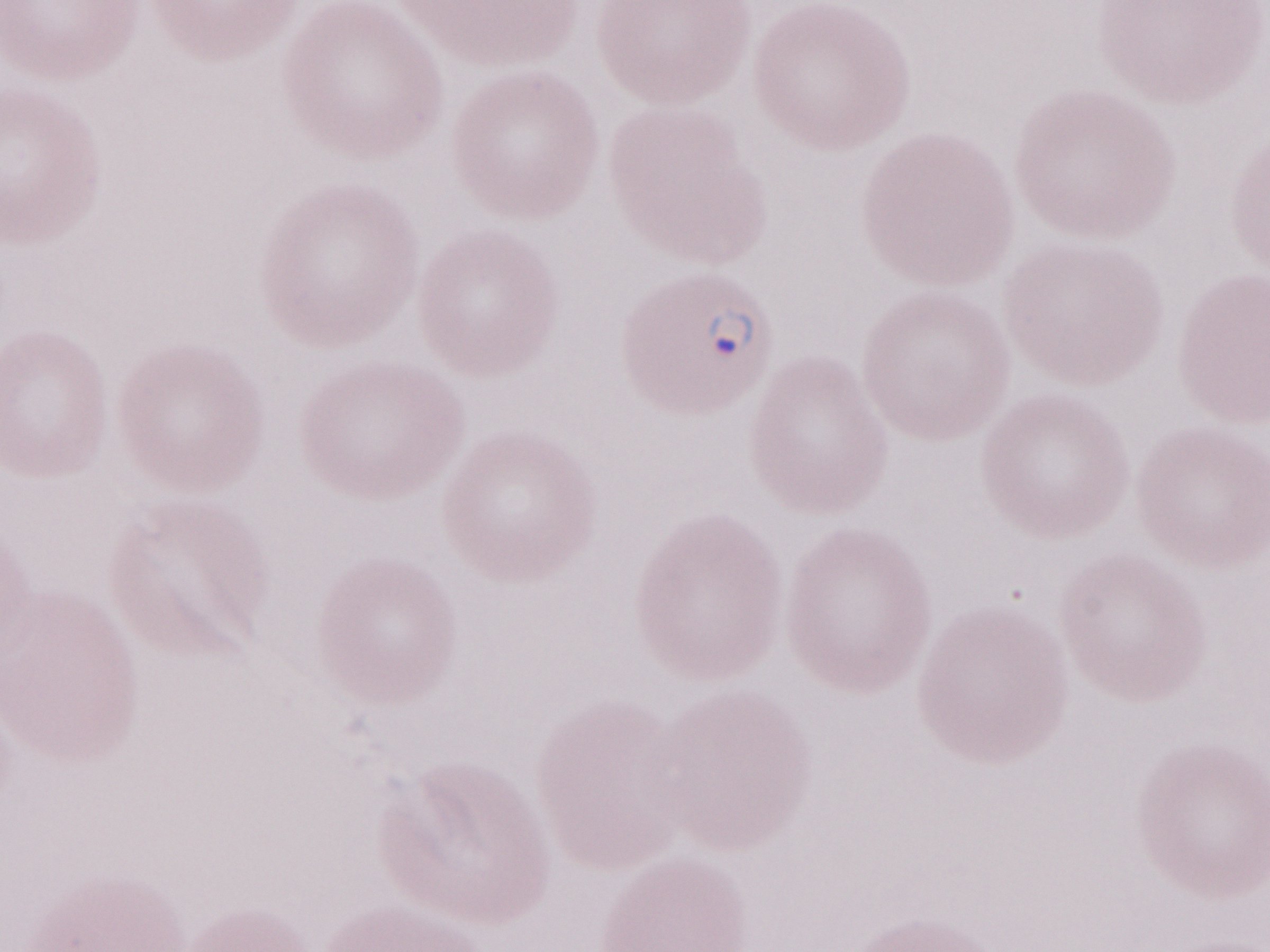
Patient-level malaria diagnosis: positive. Olympus BX43 microscope and DP73 digital camera. 1,000x magnification. Thin peripheral-blood smear. One field of this slide. May-Grünwald-Giemsa (MGG) stain. Image is 1270×952 pixels.